State the blood parasite species.
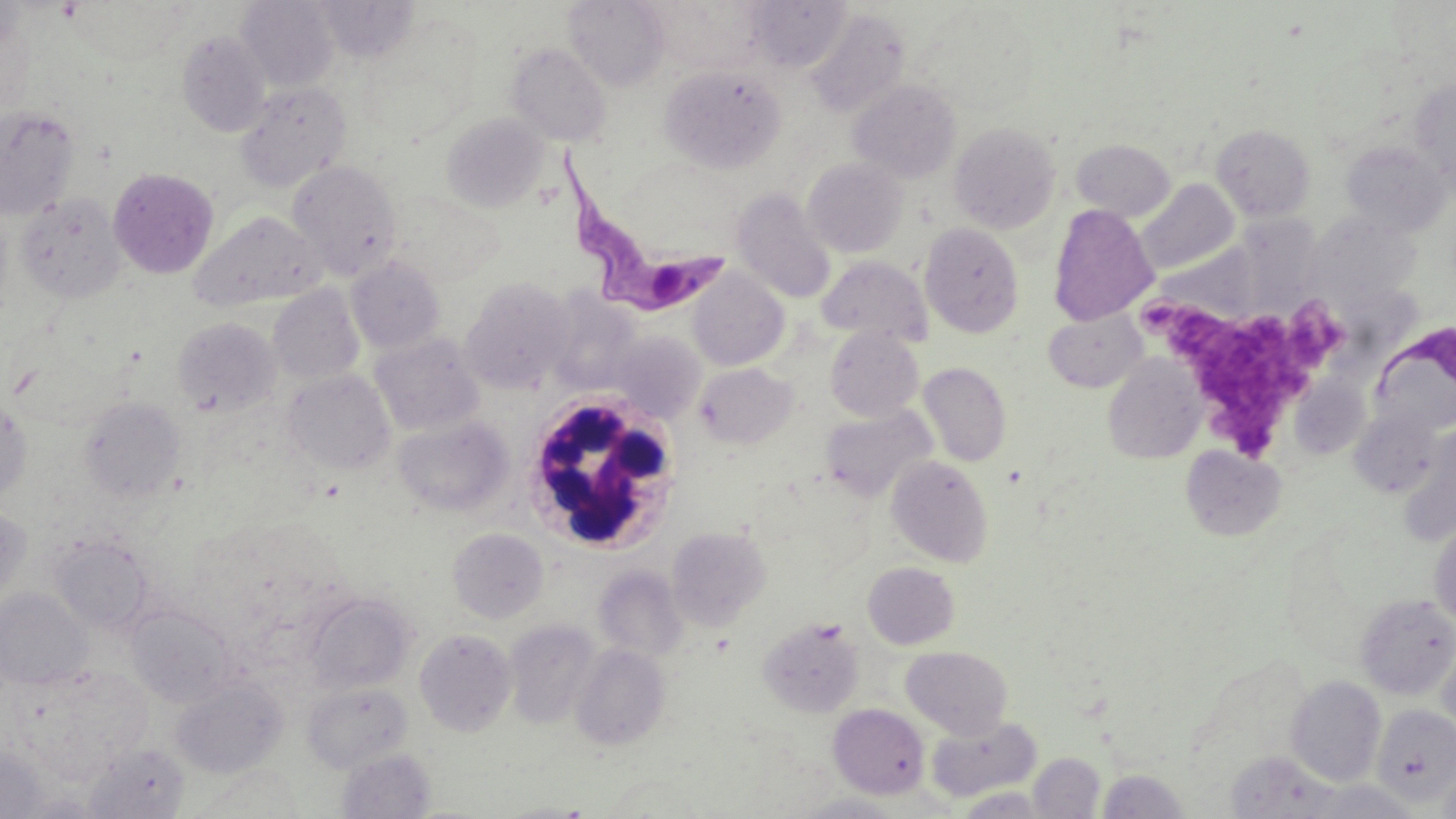

Trypanosoma brucei.

stain = May-Grünwald-Giemsa
magnification = 1000x
platelet locations = approximate bounding boxes as [x1, y1, x2, y2] in pixels: [1149, 302, 1342, 463]
field of view = one of a larger specimen
white blood cell locations = approximate bounding boxes as [x1, y1, x2, y2] in pixels: [519, 392, 685, 555]
Trypanosoma brucei locations = approximate bounding boxes as [x1, y1, x2, y2] in pixels: [555, 139, 735, 321], [1371, 322, 1456, 435]
preparation = thin blood film
modality = light microscopy
uninfected red blood cell locations = approximate bounding boxes as [x1, y1, x2, y2] in pixels: [69, 0, 190, 64], [564, 0, 671, 91], [645, 0, 764, 74], [237, 1, 339, 91], [315, 1, 421, 63], [744, 1, 850, 72], [919, 6, 1042, 114], [805, 9, 911, 119], [177, 31, 272, 137], [506, 43, 612, 146], [359, 59, 468, 144], [660, 64, 787, 173], [848, 79, 962, 183], [1410, 79, 1456, 187], [234, 81, 351, 192], [0, 106, 80, 220], [441, 113, 547, 212], [949, 122, 1061, 233], [1211, 124, 1315, 221], [1071, 139, 1175, 221], [1340, 141, 1451, 236], [803, 158, 908, 258], [287, 161, 403, 279], [108, 168, 219, 279], [1137, 179, 1239, 275], [731, 188, 837, 305], [388, 190, 500, 285], [17, 193, 128, 303], [1048, 204, 1158, 325], [189, 209, 327, 312], [1239, 210, 1326, 313], [1305, 213, 1421, 308], [919, 222, 1024, 338], [817, 255, 932, 345], [346, 256, 445, 353], [687, 270, 789, 370], [461, 277, 574, 393], [268, 285, 364, 385], [545, 293, 641, 394], [1043, 308, 1147, 393], [173, 317, 281, 416], [825, 327, 924, 422], [370, 331, 483, 436], [611, 331, 706, 422], [1103, 355, 1206, 464], [918, 362, 1012, 467], [694, 363, 797, 449], [284, 370, 396, 475], [0, 396, 31, 503], [80, 397, 185, 502], [819, 405, 936, 503], [1349, 409, 1441, 498], [393, 416, 513, 517], [1398, 425, 1456, 546], [1180, 445, 1286, 541], [885, 455, 994, 567], [0, 506, 32, 609], [1429, 517, 1456, 628], [667, 526, 770, 630], [448, 528, 549, 624], [50, 534, 154, 636], [863, 562, 960, 650], [593, 566, 688, 663], [1, 588, 92, 690], [304, 593, 415, 693], [1356, 594, 1456, 699], [126, 605, 235, 707], [759, 617, 864, 717], [504, 619, 602, 729], [415, 629, 517, 737], [1438, 638, 1456, 741], [571, 644, 670, 751], [901, 646, 1013, 738], [17, 664, 156, 779], [1286, 675, 1386, 786], [170, 678, 287, 779], [302, 682, 414, 773], [828, 703, 929, 798], [1373, 704, 1456, 804], [926, 716, 1042, 803], [85, 742, 190, 818], [0, 743, 48, 818], [336, 748, 436, 819], [1028, 752, 1105, 817], [1225, 752, 1342, 819], [1436, 760, 1456, 819], [188, 763, 304, 817], [1096, 769, 1191, 818], [1300, 780, 1421, 818], [954, 787, 1053, 818], [793, 792, 905, 818], [492, 800, 601, 817]
image size = 1456×819 pixels